Describe the morphology of the red blood cells.
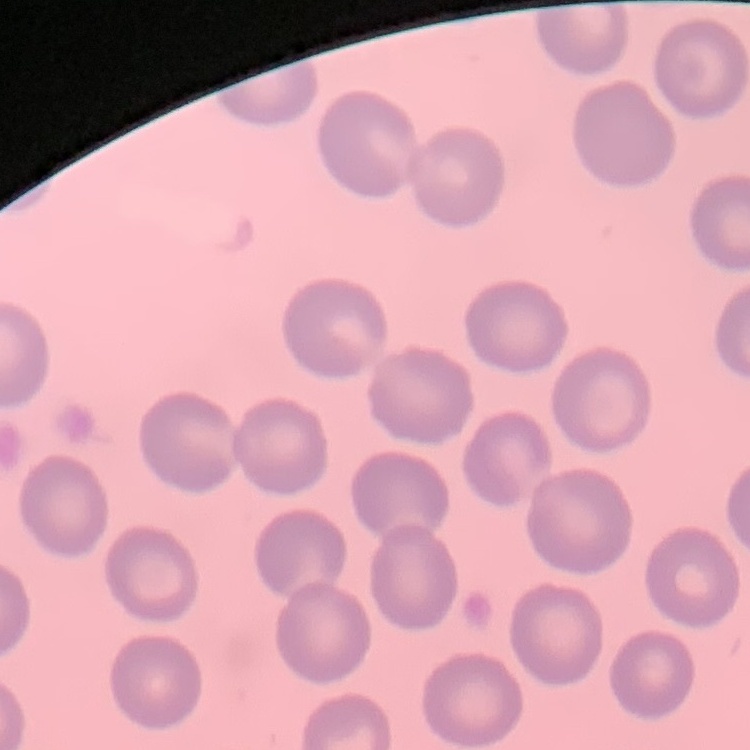

They show no rouleaux formation.

{
  "image_type": "square crop of a larger photomicrograph",
  "preparation": "thin peripheral smear",
  "stain": "Field's or Giemsa"
}